Locate every malaria parasite.
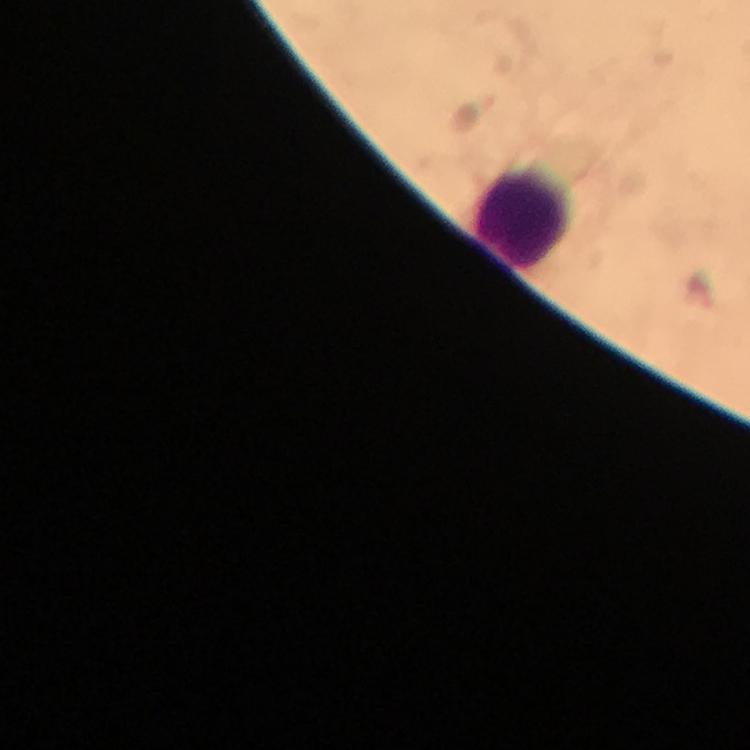

Approximate centers as [x, y] in pixels.
Malaria parasites: [699, 292].

Leukocyte locations: [521, 214]. Giemsa-stained preparation. Image is 750×750 pixels. Thick smear. Cropped region of a single field of view. 100x magnification. Immersion oil applied. Smartphone photograph taken through a microscope. From a diagnostic examination for malaria.